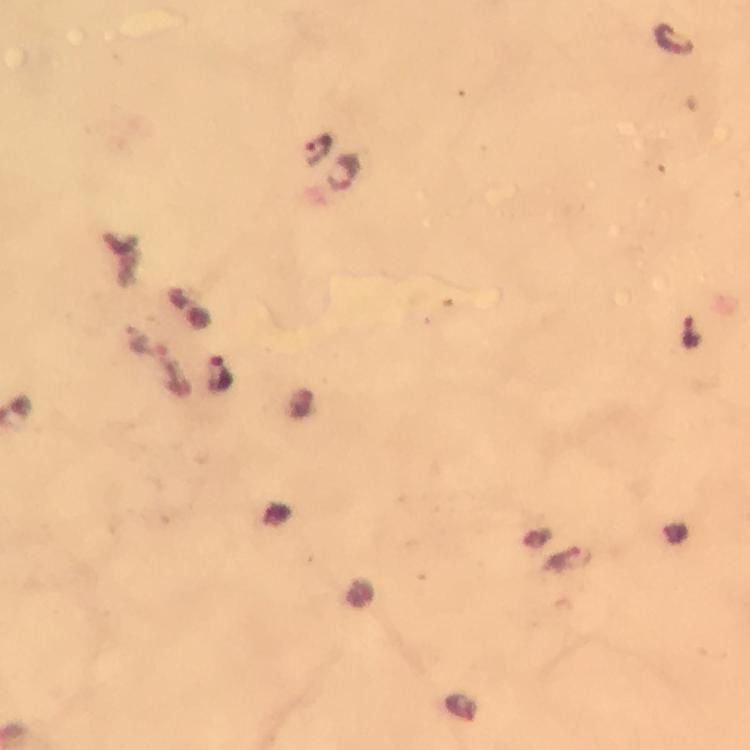

Approximate centers as {x, y} in pixels. Malaria parasite locations: {671, 40}, {318, 150}, {344, 173}, {690, 331}, {144, 346}, {218, 374}, {462, 708}. Giemsa-stained preparation. From a malaria diagnostic workup. Image is 750×750 pixels. Immersion oil was used. At 100x magnification. Cropped region of a single field of view. Smartphone photograph taken through a microscope. Thick smear.